Locate every Plasmodium parasite.
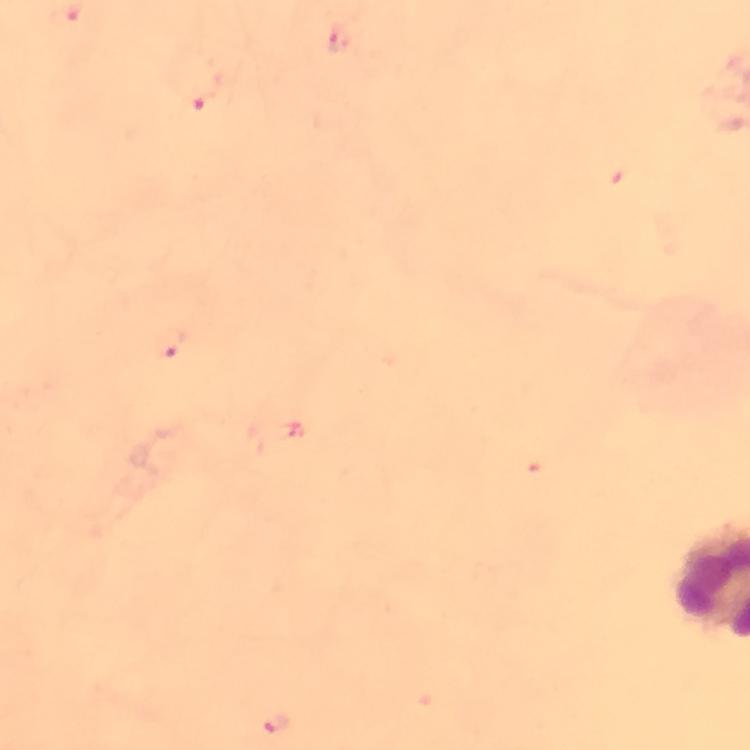
Approximate centers as (x, y) in pixels.
Plasmodium parasites: (341, 41), (201, 98), (174, 345), (276, 723).

Summary:
  - Preparation: thick smear
  - Magnification: 100x
  - Capture: smartphone photograph through a microscope
  - Cropped from: a single field of view
  - Immersion oil: applied
  - Image size: 750×750 pixels
  - Context: from a malaria diagnostic workup
  - Stain: Giemsa